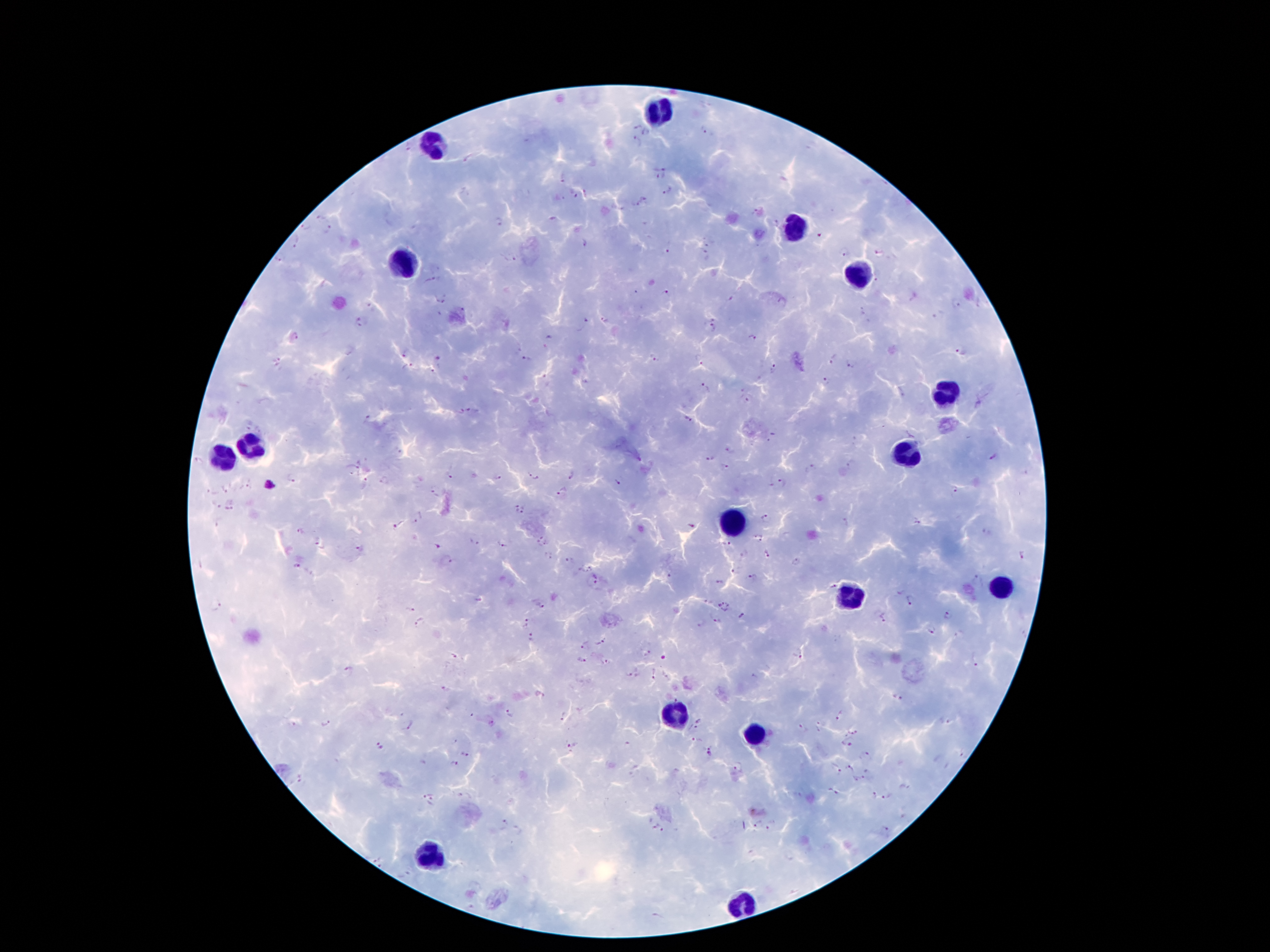
Approximate centers as [x, y] in pixels.
Summary:
  - Malaria parasite locations: [635, 126], [704, 129], [647, 132], [635, 142], [408, 147], [463, 160], [664, 172], [562, 177], [668, 191], [585, 193], [574, 197], [642, 198], [635, 206], [754, 211], [319, 218], [498, 222], [775, 223], [304, 228], [329, 229], [821, 234], [586, 242], [295, 244], [708, 244], [667, 251], [704, 253], [843, 254], [281, 258], [513, 259], [431, 280], [878, 281], [637, 292], [666, 293], [731, 299], [440, 302], [956, 304], [861, 314], [605, 320], [359, 322], [584, 324], [712, 329], [296, 337], [753, 339], [406, 352], [960, 353], [655, 358], [832, 358], [439, 359], [526, 361], [699, 361], [277, 362], [851, 364], [408, 367], [775, 368], [826, 382], [705, 387], [746, 400], [460, 411], [474, 411], [366, 419], [687, 420], [772, 438], [729, 451], [708, 457], [993, 459], [852, 464], [353, 467], [724, 467], [809, 469], [570, 475], [533, 476], [449, 477], [292, 479], [498, 479], [384, 481], [364, 482], [616, 483], [781, 484], [250, 485], [226, 488], [953, 489], [561, 491], [213, 493], [435, 493], [214, 506], [231, 506], [519, 509], [420, 518], [764, 518], [846, 523], [917, 523], [398, 525], [691, 525], [299, 531], [986, 532], [758, 538], [542, 540], [473, 542], [322, 543], [727, 544], [503, 545], [361, 547], [436, 547], [767, 554], [1022, 555], [547, 556], [567, 559], [449, 561], [796, 563], [297, 565], [585, 569], [733, 571], [670, 575], [597, 577], [753, 577], [976, 580], [718, 583], [833, 585], [911, 601], [726, 605], [217, 606], [541, 606], [410, 610], [949, 614], [743, 616], [882, 616], [527, 621], [716, 621], [700, 622], [420, 623], [931, 630], [531, 638], [601, 641], [584, 645], [647, 653], [799, 654], [455, 656], [663, 656], [581, 659], [605, 663], [976, 663], [349, 670], [654, 672], [628, 674], [667, 676], [754, 677], [444, 689], [899, 697], [677, 698], [512, 713], [839, 715], [562, 718], [699, 721], [947, 722], [294, 723], [327, 723], [492, 723], [410, 726], [818, 727], [802, 731], [854, 732], [697, 740], [846, 744], [626, 745], [709, 745], [380, 746], [571, 746], [466, 754], [710, 755], [865, 755], [964, 756], [455, 764], [740, 766], [850, 768], [834, 769], [867, 770], [300, 778], [859, 780], [428, 791], [832, 791], [872, 794], [466, 796], [887, 796], [433, 802], [502, 824], [758, 825], [773, 825], [657, 828], [886, 832], [375, 859], [406, 876], [655, 916]
  - Leukocyte locations: [656, 114], [432, 146], [795, 228], [404, 262], [856, 273], [947, 393], [252, 441], [906, 452], [220, 462], [734, 521], [1002, 589], [847, 593], [674, 716], [752, 738], [429, 854], [745, 902]
  - Magnification: 100x
  - Patient malaria status: positive for Plasmodium falciparum
  - Capture: smartphone camera through the microscope eyepiece
  - Stain: Giemsa
  - Image size: 1270×952 pixels
  - Field of view: single
  - Preparation: thick blood film